Give the position of every Plasmodium parasite.
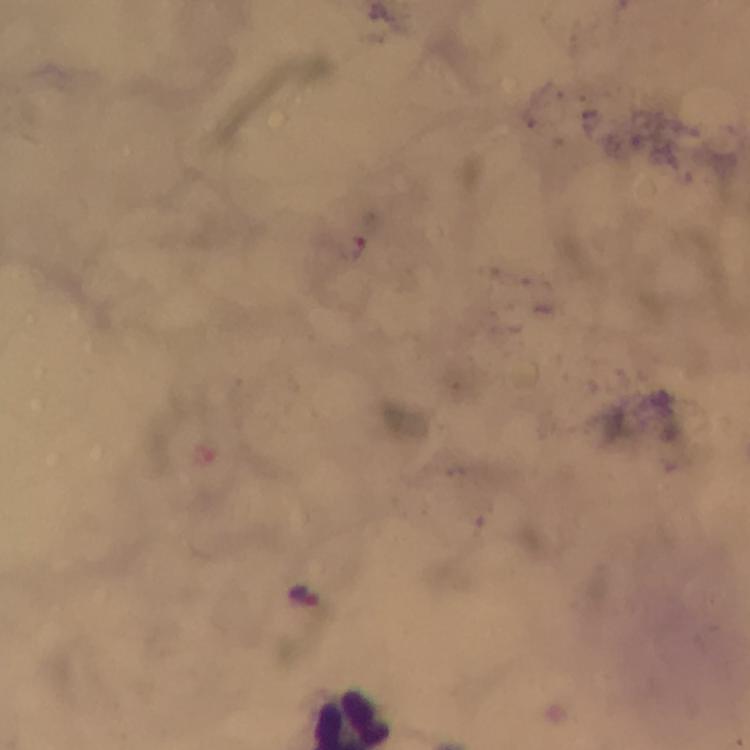
Approximate centers as (x, y) in pixels.
Plasmodium parasites: (306, 598).

stain = Giemsa
image size = 750×750 pixels
cropped from = a single field of view
preparation = thick smear
immersion oil = applied
magnification = 100x
context = from a diagnostic examination for malaria
capture = smartphone mounted on the microscope